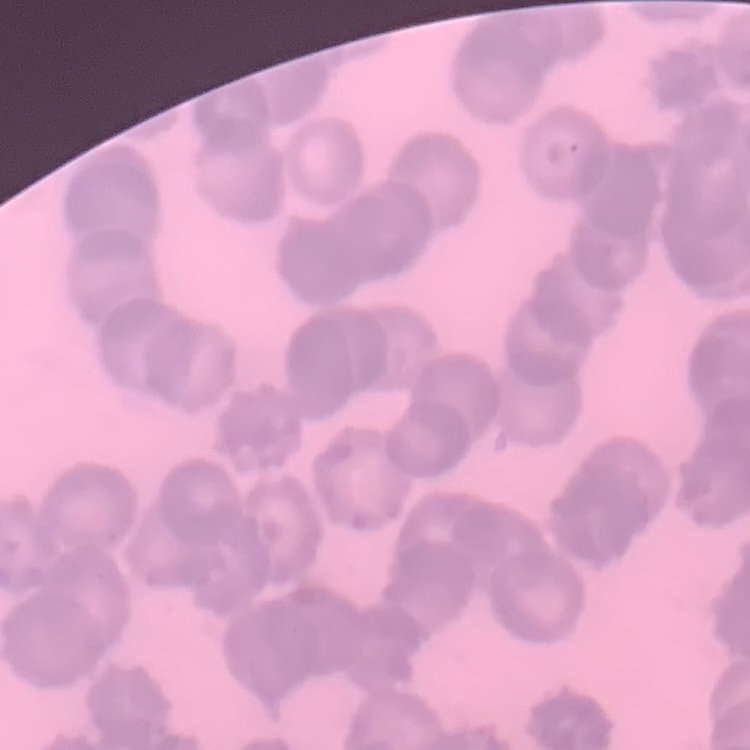
erythrocyte morphology = rouleaux formation
preparation = thin blood film
stain = Field's or Giemsa
image type = one tile cut from a larger photomicrograph